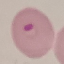
Summary:
  - Result: malaria parasites identified
  - Image type: automatically extracted cell patch, resized to 64 × 64 pixels
  - Preparation: thin blood smear
  - Stain: Giemsa
  - Capture: smartphone through the microscope eyepiece